Classify this cell by malaria status.
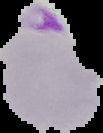
It is parasitized.

Summary:
  - Image size: 103×133 pixels
  - Image type: segmented cell region with the area outside set to black
  - Preparation: thin blood smear